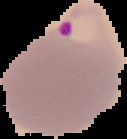
Summary:
  - Preparation: thin blood smear
  - Malaria status: parasitized
  - Image type: segmented cell region with the area outside set to black
  - Image size: 127×139 pixels